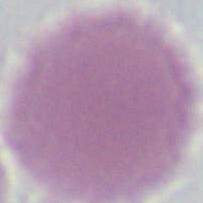

modality = micrograph
identification = red blood cell
magnification = 1000x